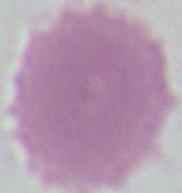

Summary:
  - Identification: erythrocyte
  - Modality: micrograph
  - Magnification: 1000x